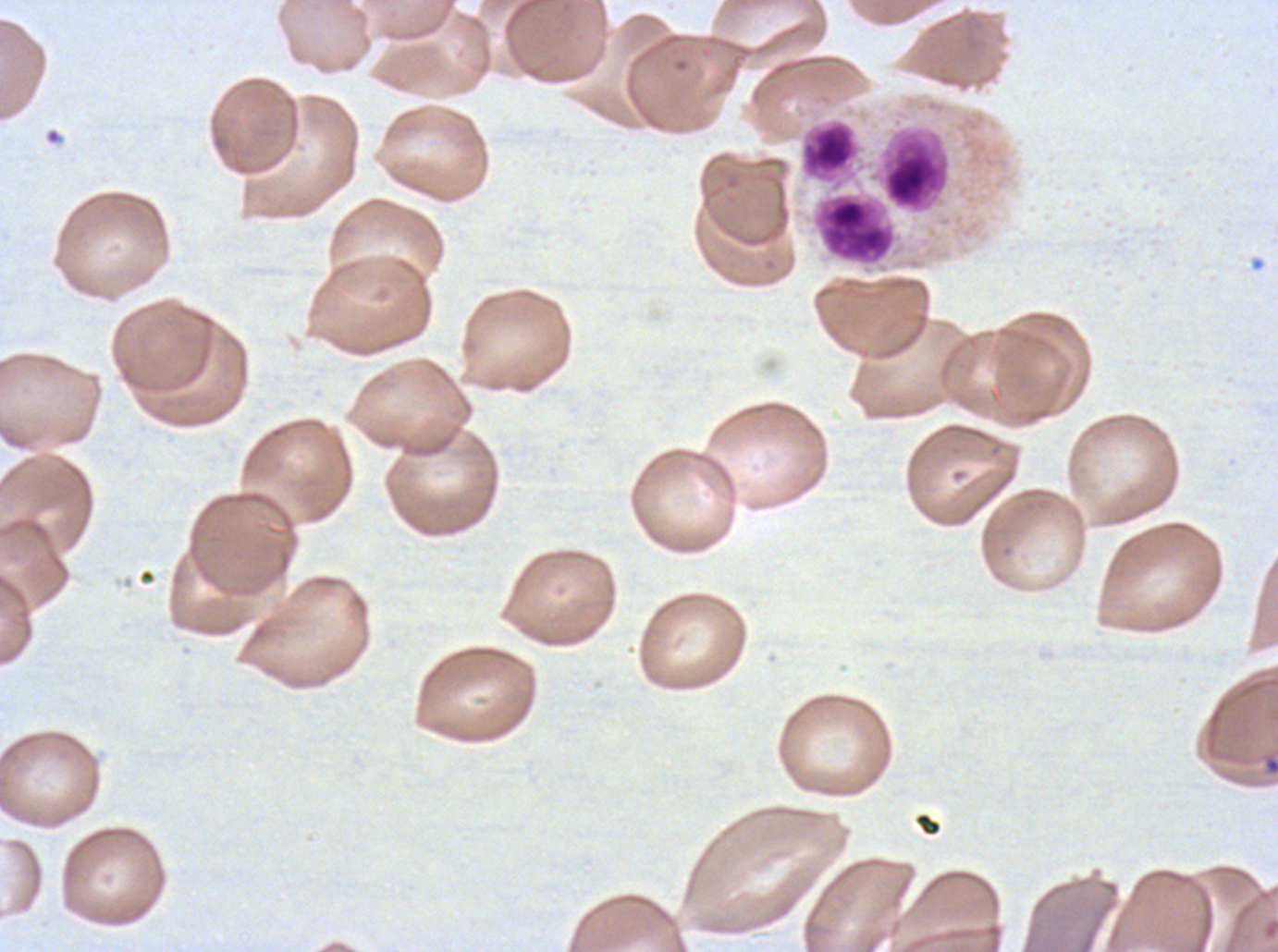

{
  "image_size": "1278×952 pixels",
  "specimen": "Plasmodium falciparum from a patient in The Gambia, cultured ex vivo for 24 to 48 hours",
  "stain": "Giemsa",
  "field_of_view": "sub-image separated from a larger composite",
  "leukocyte_locations": "approximate bounding boxes as (x1, y1, x2, y2) in pixels: (800, 119, 860, 183), (876, 127, 952, 214), (815, 193, 896, 265)",
  "preparation": "thin blood film"
}